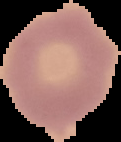
Summary:
  - Preparation: thin blood smear
  - Image size: 121×142 pixels
  - Image type: segmented cell region with the area outside set to black
  - Malaria status: uninfected